Assess this cell for malaria.
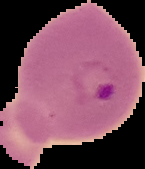
It is parasitized.

Summary:
  - Image type: segmented cell region on a black background
  - Preparation: thin blood smear
  - Image size: 145×169 pixels